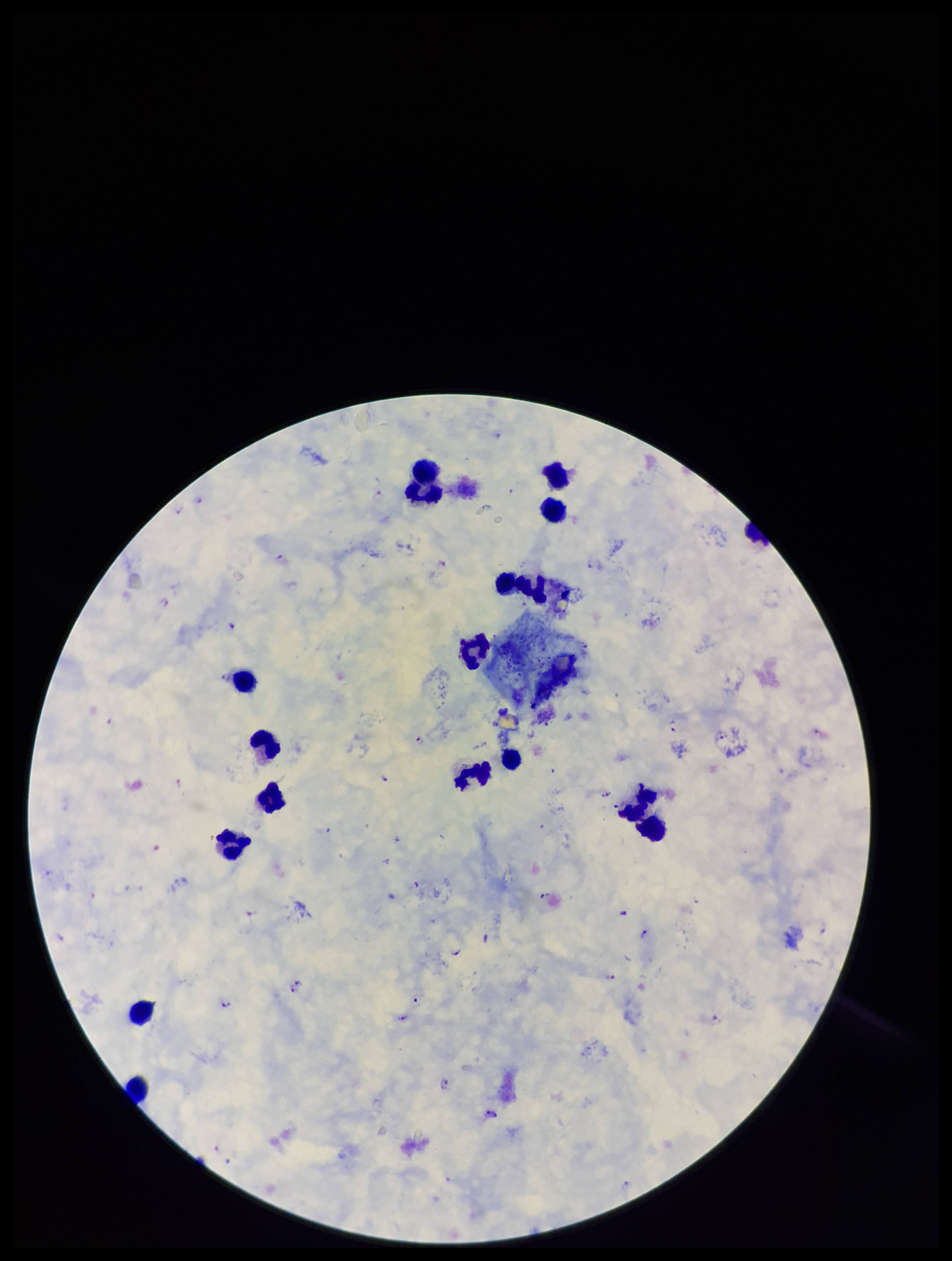
species reported for this patient = Plasmodium falciparum
Plasmodium parasites = detected
patient malaria status = infected
parasite count = 27
preparation = thick blood smear
capture = smartphone photograph through the microscope eyepiece
stain = Giemsa
field of view = one from this slide
leukocyte count = 18
image size = 952×1261 pixels